Classify this cell by malaria status.
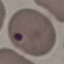
It is uninfected.

Thin blood smear. Acquired by smartphone through the microscope eyepiece. Giemsa-stained preparation. Cell patch, automatically extracted from a larger field of view and resized to 64 × 64 pixels.